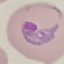

{
  "malaria_status": "parasitized",
  "capture": "smartphone through the microscope eyepiece",
  "preparation": "thin blood film",
  "image_type": "cell patch, automatically extracted from a larger field of view and resized to 64 × 64 pixels",
  "stain": "Giemsa"
}